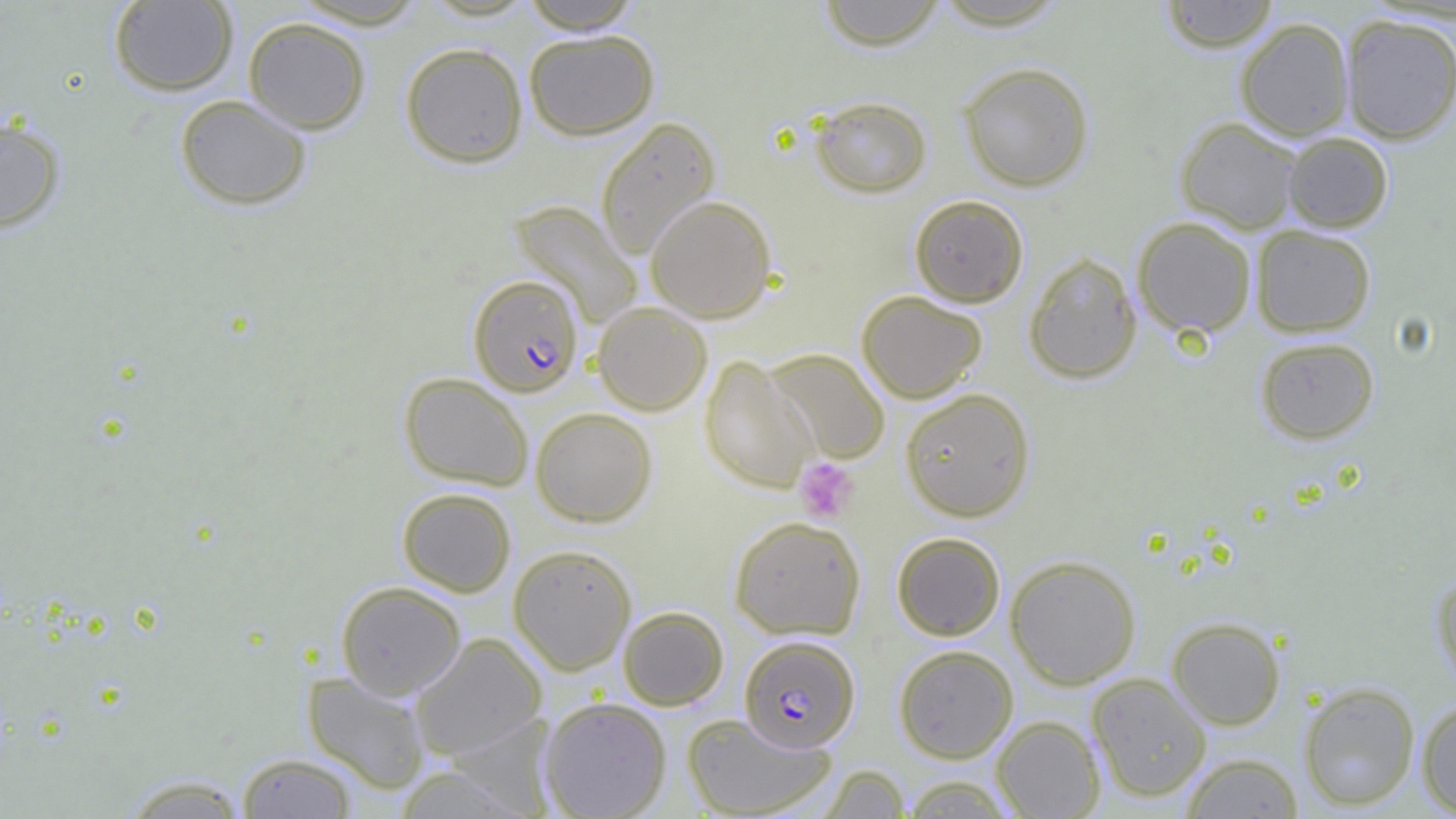
Summary:
  - Coordinate format: approximate bounding boxes as (x1,y1)-(x2,y2) corner pairs in pixels
  - Uninfected red blood cell locations: (108,0)-(239,96), (518,0)-(644,34), (817,0)-(948,51), (1159,0)-(1279,53), (1339,14)-(1456,144), (243,17)-(371,134), (1235,17)-(1354,141), (523,29)-(659,140), (400,42)-(528,168), (957,61)-(1094,192), (174,94)-(313,211), (810,95)-(933,198), (595,116)-(720,260), (1175,116)-(1303,234), (0,117)-(67,234), (1282,132)-(1394,233), (645,194)-(777,323), (909,194)-(1029,307), (509,199)-(644,330), (1132,217)-(1258,338), (1250,224)-(1376,337), (1023,251)-(1142,384), (856,290)-(988,403), (592,301)-(712,416), (1254,336)-(1380,444), (764,348)-(890,464), (699,356)-(819,494), (399,372)-(534,491), (899,387)-(1035,521), (530,406)-(658,527), (397,487)-(516,597), (729,516)-(866,640), (892,531)-(1005,641), (508,544)-(637,674), (1005,554)-(1141,689), (1431,572)-(1456,692), (336,581)-(466,699), (617,606)-(729,710), (1166,616)-(1286,730), (409,633)-(548,761), (893,644)-(1018,763), (301,671)-(432,794), (1087,672)-(1211,802), (1298,681)-(1420,811), (539,697)-(672,818), (1415,698)-(1456,816), (681,712)-(836,818), (991,715)-(1106,818), (236,752)-(358,818), (1179,753)-(1304,818), (393,764)-(535,818), (817,764)-(910,818), (119,773)-(252,818), (899,775)-(1019,817)
  - Platelet locations: (794,456)-(860,524)
  - Plasmodium falciparum-infected red blood cell locations: (467,274)-(584,397), (738,635)-(860,752)
  - Slide-level diagnosis: Plasmodium falciparum
  - Field of view: single
  - Preparation: thin blood smear
  - Modality: light microscopy
  - Magnification: 1000x
  - Image size: 1456×819 pixels